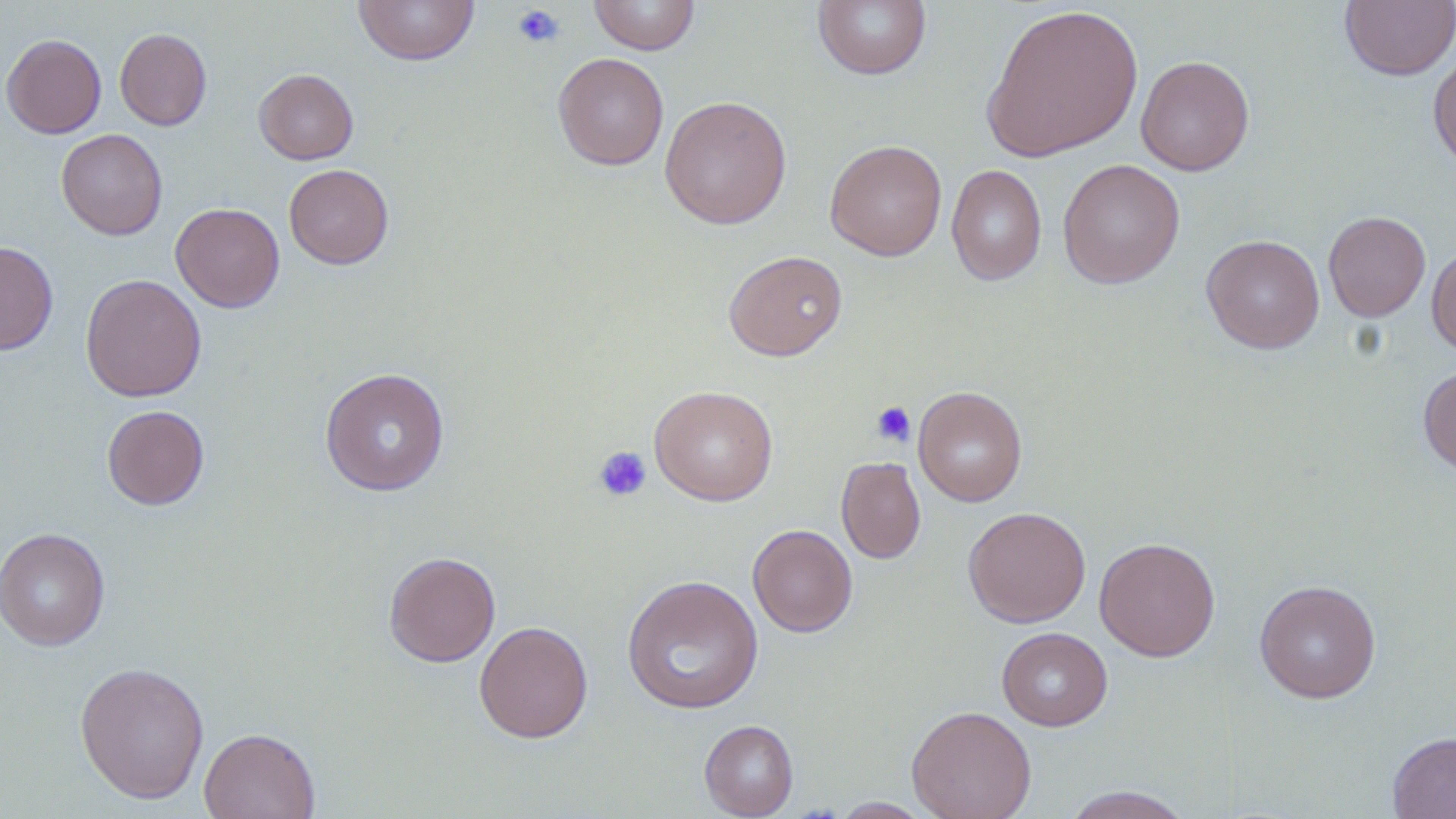
slide-level diagnosis = negative for blood parasites
image size = 1456×819 pixels
stain = May-Grünwald-Giemsa
magnification = 1000x
preparation = thin blood film
uninfected red blood cell locations = approximate bounding boxes as [x1, y1, x2, y2] in pixels: [353, 0, 480, 66], [588, 0, 701, 55], [1340, 0, 1456, 81], [812, 1, 932, 81], [981, 4, 1144, 162], [115, 28, 212, 130], [1, 34, 106, 138], [1428, 48, 1456, 171], [553, 52, 669, 170], [1136, 55, 1255, 176], [254, 68, 358, 164], [659, 94, 793, 230], [56, 128, 168, 240], [824, 140, 947, 261], [1058, 159, 1184, 288], [283, 164, 394, 269], [946, 164, 1047, 286], [170, 202, 285, 312], [1323, 211, 1431, 322], [1201, 234, 1325, 353], [0, 241, 58, 355], [1426, 245, 1456, 357], [724, 250, 848, 361], [80, 273, 206, 402], [1418, 363, 1456, 477], [319, 367, 450, 496], [650, 385, 778, 505], [913, 386, 1027, 506], [102, 405, 210, 510], [836, 456, 926, 564], [963, 506, 1091, 627], [747, 524, 858, 637], [0, 527, 110, 651], [1094, 537, 1221, 661], [383, 551, 501, 667], [622, 574, 764, 715], [1253, 579, 1382, 703], [474, 621, 594, 743], [996, 627, 1113, 731], [74, 660, 210, 804], [906, 705, 1036, 819], [699, 719, 798, 818], [199, 727, 321, 819], [1387, 731, 1456, 818], [1061, 786, 1196, 818], [830, 797, 933, 818]
field of view = single
platelet locations = approximate bounding boxes as [x1, y1, x2, y2] in pixels: [511, 4, 565, 49], [871, 402, 916, 447], [593, 445, 652, 502]
modality = optical microscopy